Assess the morphology of the erythrocytes.
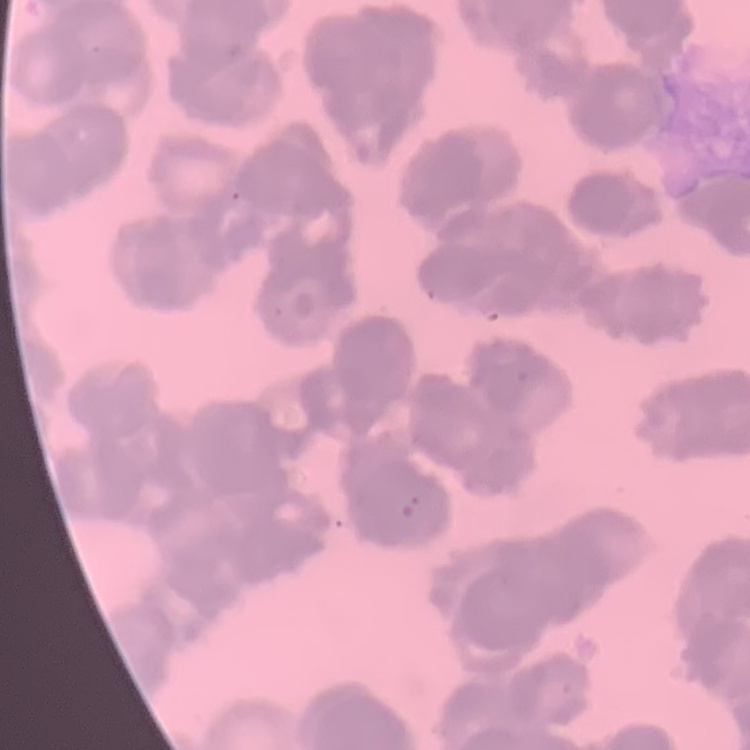

They show rouleaux formation.

{
  "stain": "Field's or Giemsa",
  "image_type": "square crop of a larger photomicrograph",
  "preparation": "thin blood smear"
}